Report the malaria status of this cell.
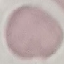

Uninfected.

capture = smartphone through the microscope eyepiece
image type = automatically extracted cell patch, resized to 64 × 64 pixels
preparation = thin smear
stain = Giemsa